Assess this cell for malaria.
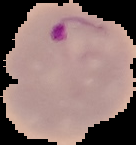

It is parasitized.

image size = 136×145 pixels
image type = cell region segmented out of the field of view; surrounding area masked to black
preparation = thin blood film